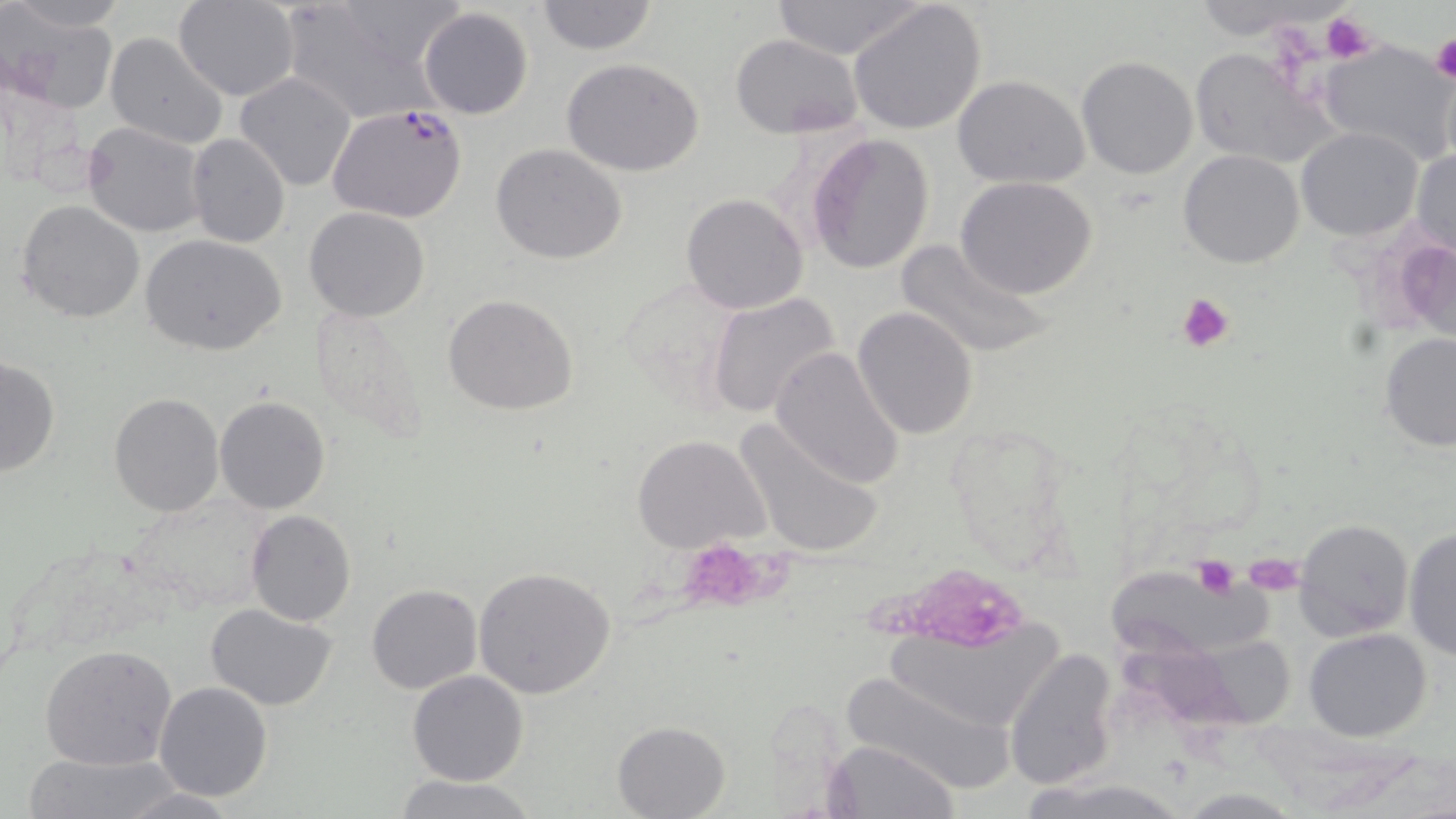
Approximate bounding boxes as named x1/y1/x2/y2 corners in pixels. Plasmodium falciparum-infected red blood cell locations: (x1=327, y1=106, x2=468, y2=224). Uninfected red blood cell locations: (x1=8, y1=0, x2=127, y2=30), (x1=175, y1=0, x2=299, y2=101), (x1=275, y1=0, x2=452, y2=118), (x1=536, y1=0, x2=658, y2=56), (x1=770, y1=0, x2=930, y2=60), (x1=848, y1=2, x2=989, y2=137), (x1=418, y1=7, x2=534, y2=120), (x1=6, y1=15, x2=118, y2=113), (x1=106, y1=32, x2=229, y2=149), (x1=730, y1=34, x2=864, y2=138), (x1=1318, y1=38, x2=1453, y2=165), (x1=1187, y1=48, x2=1334, y2=167), (x1=1077, y1=55, x2=1199, y2=179), (x1=560, y1=58, x2=704, y2=177), (x1=234, y1=72, x2=357, y2=192), (x1=951, y1=74, x2=1090, y2=189), (x1=82, y1=121, x2=207, y2=238), (x1=1296, y1=128, x2=1422, y2=241), (x1=805, y1=131, x2=936, y2=274), (x1=186, y1=132, x2=290, y2=248), (x1=490, y1=144, x2=627, y2=264), (x1=1411, y1=146, x2=1456, y2=259), (x1=1177, y1=149, x2=1304, y2=269), (x1=956, y1=177, x2=1099, y2=298), (x1=681, y1=193, x2=809, y2=315), (x1=17, y1=200, x2=146, y2=322), (x1=303, y1=207, x2=430, y2=322), (x1=140, y1=235, x2=288, y2=356), (x1=1388, y1=237, x2=1455, y2=339), (x1=893, y1=238, x2=1055, y2=362), (x1=615, y1=274, x2=748, y2=404), (x1=442, y1=293, x2=578, y2=415), (x1=708, y1=293, x2=842, y2=423), (x1=309, y1=304, x2=432, y2=447), (x1=852, y1=305, x2=980, y2=441), (x1=1379, y1=330, x2=1456, y2=452), (x1=770, y1=347, x2=907, y2=489), (x1=0, y1=356, x2=59, y2=478), (x1=108, y1=392, x2=225, y2=517), (x1=213, y1=395, x2=332, y2=515), (x1=732, y1=416, x2=886, y2=560), (x1=631, y1=434, x2=769, y2=552), (x1=246, y1=510, x2=356, y2=626), (x1=1294, y1=518, x2=1414, y2=639), (x1=1403, y1=526, x2=1456, y2=662), (x1=474, y1=565, x2=617, y2=702), (x1=1109, y1=566, x2=1272, y2=654), (x1=366, y1=583, x2=483, y2=695), (x1=207, y1=604, x2=338, y2=710), (x1=879, y1=615, x2=1064, y2=727), (x1=1304, y1=628, x2=1432, y2=743), (x1=40, y1=643, x2=179, y2=772), (x1=1113, y1=647, x2=1306, y2=732), (x1=1004, y1=648, x2=1121, y2=789), (x1=838, y1=668, x2=1016, y2=794), (x1=407, y1=670, x2=529, y2=786), (x1=154, y1=681, x2=273, y2=803), (x1=612, y1=721, x2=728, y2=818), (x1=826, y1=739, x2=961, y2=819), (x1=22, y1=752, x2=187, y2=819), (x1=392, y1=774, x2=536, y2=819), (x1=1026, y1=777, x2=1193, y2=817), (x1=111, y1=782, x2=246, y2=819). Platelet locations: (x1=1319, y1=12, x2=1377, y2=65), (x1=1429, y1=35, x2=1456, y2=83), (x1=1177, y1=291, x2=1235, y2=353), (x1=679, y1=538, x2=786, y2=615), (x1=1244, y1=551, x2=1303, y2=596), (x1=1190, y1=557, x2=1241, y2=600), (x1=889, y1=572, x2=1023, y2=639). Slide-level diagnosis: Plasmodium falciparum. May-Grünwald-Giemsa stain. Thin blood smear. Optical microscopy. Image is 1456×819 pixels. Captured at 1000x magnification. One field of a larger specimen.